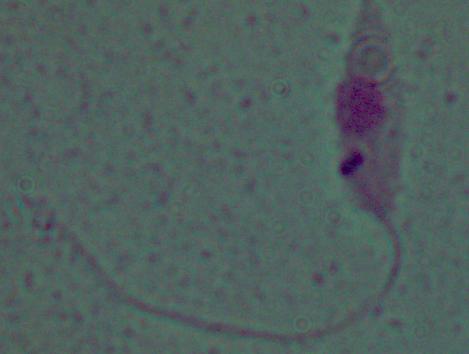

{
  "modality": "micrograph",
  "magnification": "1000x",
  "identification": "Leishmania"
}